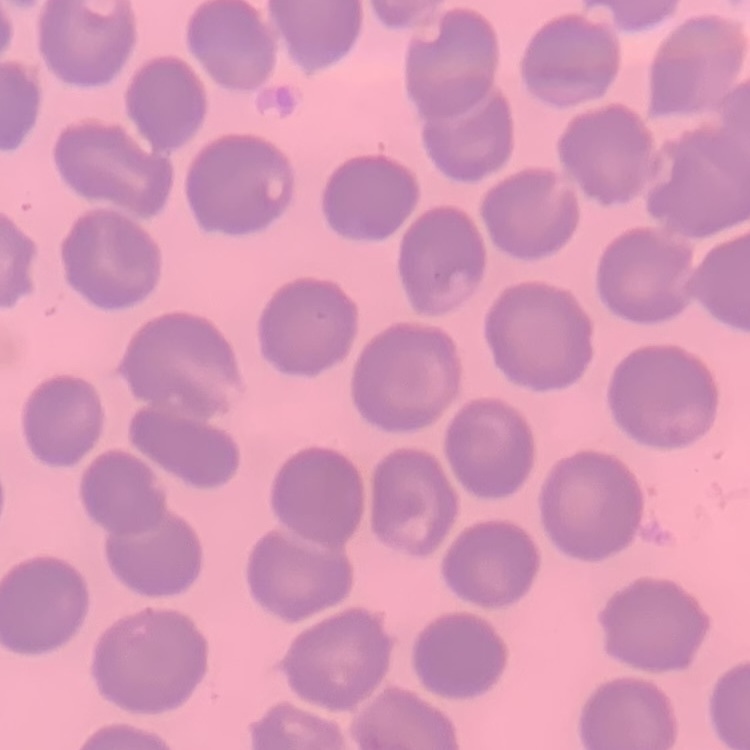
{
  "red_blood_cell_morphology": "no rouleaux formation",
  "stain": "Field's or Giemsa",
  "image_type": "one tile cut from a larger photomicrograph",
  "preparation": "thin peripheral smear"
}